Report the malaria status of this cell.
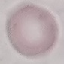

Uninfected.

Automatically extracted cell patch, resized to 64 × 64 pixels. Acquired by smartphone through the microscope eyepiece. Giemsa stain. Thin blood smear.